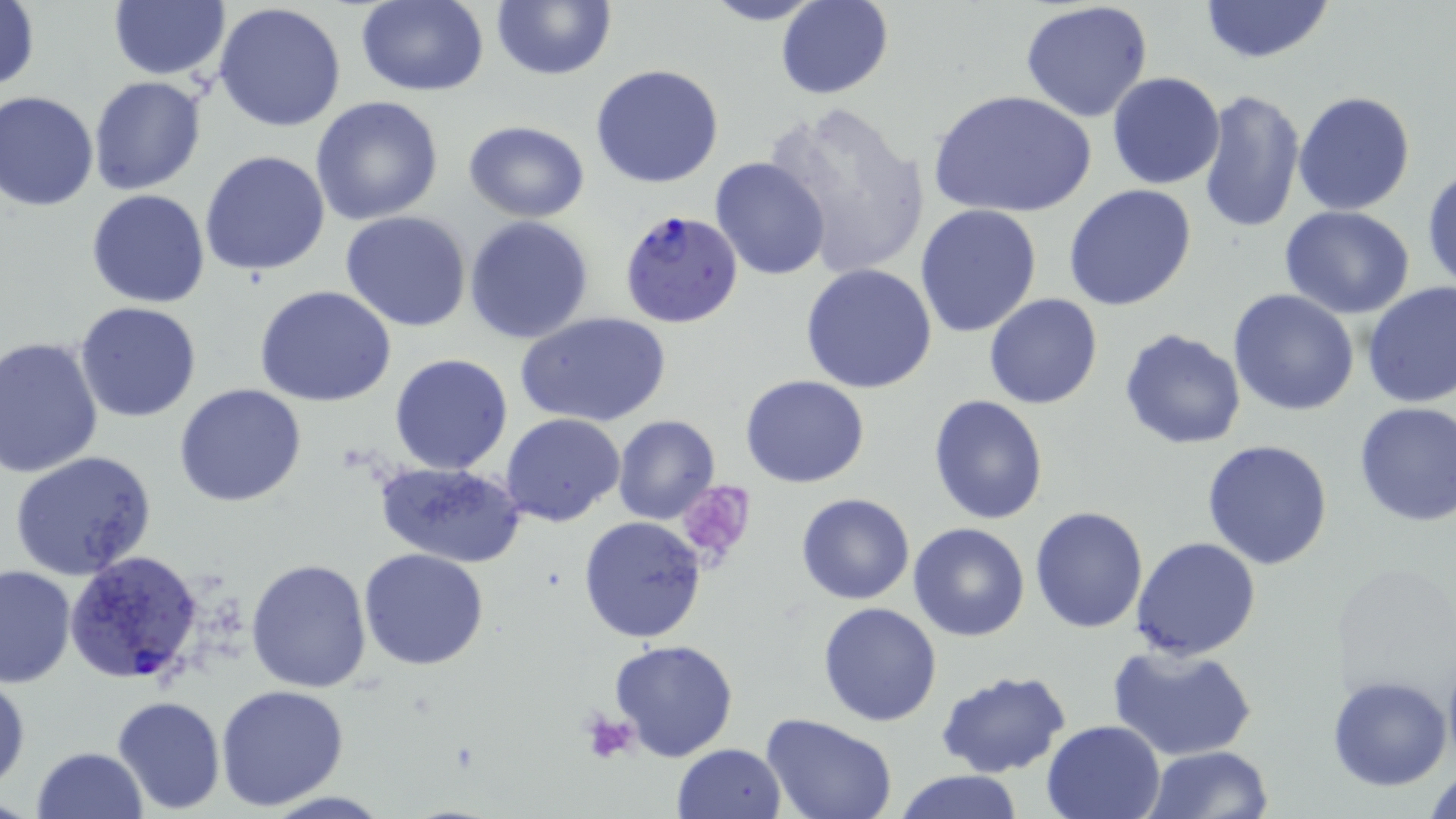

slide-level diagnosis = Plasmodium falciparum
modality = optical microscopy
preparation = thin blood film
uninfected red blood cell locations = approximate bounding boxes as named x1/y1/x2/y2 corners in pixels: (x1=107, y1=0, x2=229, y2=81), (x1=490, y1=0, x2=616, y2=81), (x1=701, y1=0, x2=830, y2=26), (x1=775, y1=0, x2=893, y2=100), (x1=1020, y1=0, x2=1154, y2=121), (x1=0, y1=1, x2=41, y2=93), (x1=354, y1=1, x2=489, y2=95), (x1=1199, y1=1, x2=1334, y2=65), (x1=214, y1=3, x2=347, y2=133), (x1=590, y1=63, x2=725, y2=189), (x1=1106, y1=72, x2=1225, y2=190), (x1=87, y1=75, x2=207, y2=196), (x1=930, y1=89, x2=1095, y2=222), (x1=1198, y1=89, x2=1306, y2=233), (x1=1294, y1=89, x2=1417, y2=214), (x1=0, y1=91, x2=100, y2=211), (x1=311, y1=96, x2=444, y2=226), (x1=764, y1=99, x2=931, y2=281), (x1=463, y1=120, x2=589, y2=222), (x1=200, y1=151, x2=331, y2=277), (x1=709, y1=156, x2=832, y2=281), (x1=1423, y1=166, x2=1456, y2=292), (x1=1062, y1=184, x2=1197, y2=310), (x1=86, y1=191, x2=211, y2=308), (x1=914, y1=204, x2=1043, y2=339), (x1=1279, y1=205, x2=1415, y2=319), (x1=340, y1=210, x2=474, y2=332), (x1=464, y1=216, x2=594, y2=344), (x1=799, y1=263, x2=938, y2=394), (x1=1361, y1=282, x2=1456, y2=409), (x1=255, y1=286, x2=398, y2=408), (x1=1228, y1=288, x2=1359, y2=416), (x1=984, y1=293, x2=1103, y2=410), (x1=74, y1=301, x2=202, y2=422), (x1=516, y1=310, x2=672, y2=427), (x1=1120, y1=326, x2=1246, y2=450), (x1=0, y1=337, x2=103, y2=478), (x1=389, y1=353, x2=515, y2=475), (x1=741, y1=375, x2=869, y2=488), (x1=174, y1=382, x2=306, y2=507), (x1=928, y1=394, x2=1049, y2=525), (x1=1353, y1=400, x2=1455, y2=526), (x1=501, y1=414, x2=625, y2=527), (x1=614, y1=416, x2=720, y2=524), (x1=1202, y1=440, x2=1334, y2=571), (x1=9, y1=450, x2=157, y2=579), (x1=375, y1=460, x2=526, y2=567), (x1=795, y1=493, x2=917, y2=605), (x1=1029, y1=505, x2=1148, y2=633), (x1=579, y1=515, x2=707, y2=642), (x1=908, y1=522, x2=1031, y2=641), (x1=1130, y1=537, x2=1262, y2=660), (x1=359, y1=548, x2=489, y2=670), (x1=245, y1=559, x2=371, y2=693), (x1=0, y1=564, x2=75, y2=687), (x1=816, y1=601, x2=942, y2=727), (x1=607, y1=639, x2=739, y2=761), (x1=1106, y1=642, x2=1258, y2=761), (x1=934, y1=669, x2=1072, y2=779), (x1=0, y1=671, x2=29, y2=793), (x1=1327, y1=674, x2=1451, y2=791), (x1=215, y1=684, x2=351, y2=811), (x1=112, y1=694, x2=225, y2=815), (x1=759, y1=714, x2=899, y2=819), (x1=1041, y1=719, x2=1167, y2=819), (x1=671, y1=742, x2=787, y2=819), (x1=1141, y1=744, x2=1275, y2=819), (x1=31, y1=746, x2=147, y2=819), (x1=1424, y1=760, x2=1455, y2=819), (x1=894, y1=769, x2=1024, y2=819)
stain = May-Grünwald-Giemsa
magnification = 1000x
Plasmodium falciparum-infected red blood cell locations = approximate bounding boxes as named x1/y1/x2/y2 corners in pixels: (x1=619, y1=211, x2=746, y2=329), (x1=66, y1=550, x2=204, y2=687)
field of view = one of a larger specimen
platelet locations = approximate bounding boxes as named x1/y1/x2/y2 corners in pixels: (x1=677, y1=479, x2=759, y2=566), (x1=579, y1=709, x2=641, y2=768)
image size = 1456×819 pixels